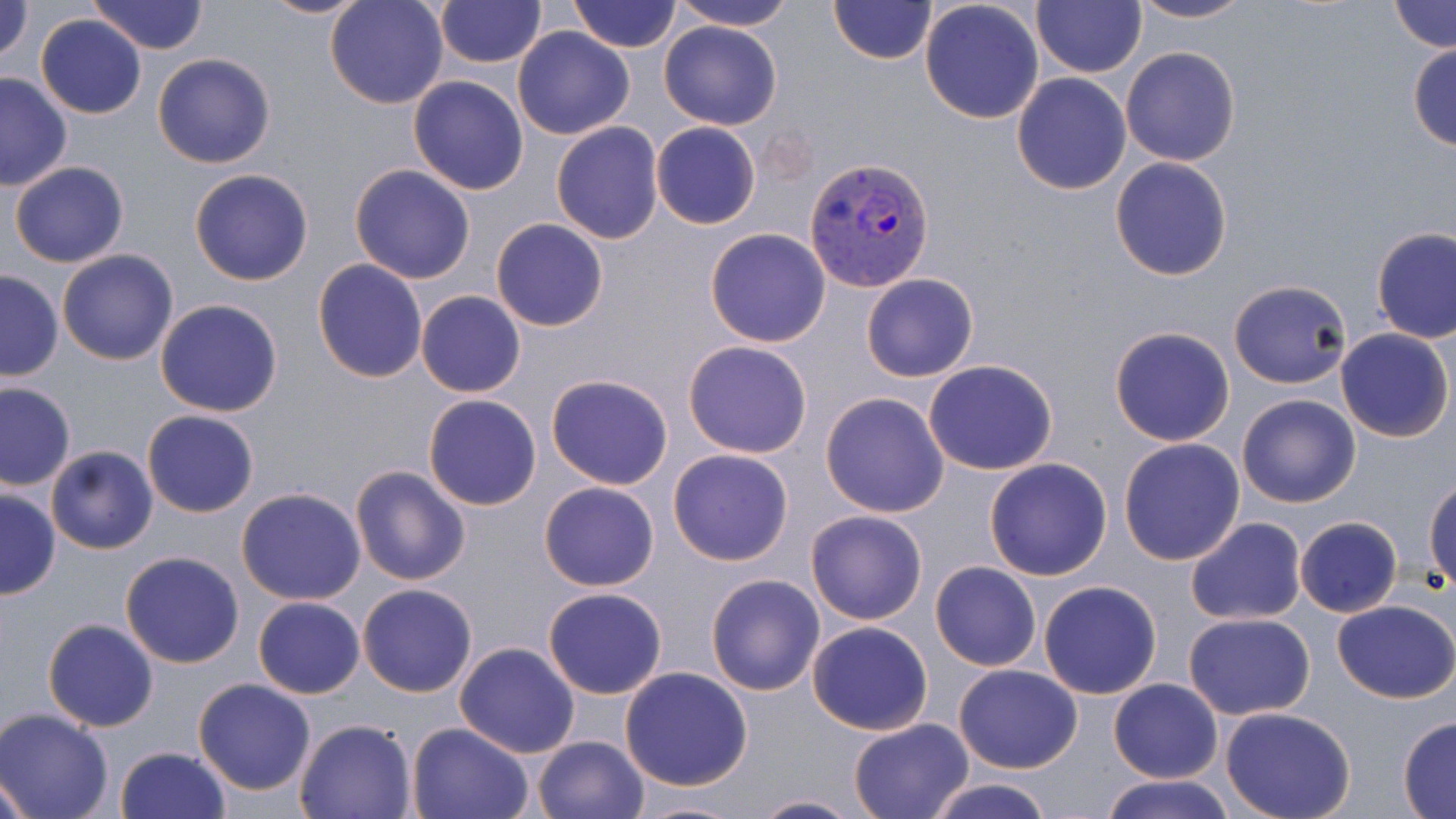 Approximate bounding boxes as (x1, y1, x2, y2) in pixels. Uninfected red blood cell locations: (0, 0, 34, 64), (88, 0, 209, 54), (257, 0, 370, 18), (324, 0, 451, 109), (433, 0, 544, 68), (569, 0, 683, 54), (670, 0, 798, 31), (828, 0, 938, 66), (839, 0, 1011, 90), (1032, 0, 1146, 78), (1127, 0, 1257, 25), (919, 1, 1045, 124), (1389, 1, 1454, 52), (36, 13, 147, 119), (658, 20, 782, 130), (512, 27, 635, 141), (1408, 42, 1456, 151), (1121, 46, 1240, 166), (151, 54, 275, 170), (0, 71, 74, 192), (1011, 72, 1132, 195), (408, 75, 529, 194), (550, 121, 665, 244), (651, 122, 761, 229), (1110, 157, 1233, 280), (9, 160, 129, 268), (349, 164, 475, 283), (189, 169, 314, 286), (491, 219, 609, 332), (1372, 227, 1456, 343), (704, 228, 832, 348), (57, 249, 179, 366), (312, 260, 427, 384), (0, 270, 64, 381), (861, 273, 979, 382), (1227, 280, 1354, 388), (416, 290, 525, 398), (154, 298, 283, 417), (1109, 326, 1235, 446), (1334, 328, 1453, 443), (683, 339, 813, 458), (923, 359, 1059, 475), (545, 373, 674, 490), (0, 380, 75, 491), (820, 392, 950, 517), (423, 393, 543, 510), (1236, 393, 1360, 509), (142, 408, 259, 519), (1119, 438, 1245, 565), (45, 443, 159, 555), (668, 448, 794, 567), (983, 458, 1113, 580), (349, 465, 470, 585), (1425, 477, 1456, 589), (539, 481, 659, 592), (0, 488, 61, 600), (236, 489, 366, 605), (805, 509, 929, 626), (1295, 516, 1402, 619), (1185, 518, 1308, 623), (120, 551, 245, 669), (930, 562, 1041, 671), (705, 572, 826, 695), (1037, 580, 1163, 700), (357, 583, 479, 698), (542, 586, 668, 699), (253, 596, 364, 699), (1332, 600, 1456, 703), (1183, 613, 1315, 719), (44, 618, 158, 731), (806, 621, 933, 736), (454, 641, 581, 757), (952, 664, 1083, 774), (619, 667, 754, 791), (192, 677, 318, 799), (1108, 679, 1223, 783), (1220, 708, 1355, 819), (0, 710, 116, 819), (294, 717, 418, 818), (847, 717, 975, 819), (1398, 717, 1456, 817), (404, 721, 534, 819), (532, 735, 652, 819), (115, 744, 231, 819), (1, 773, 32, 818), (1101, 773, 1237, 819), (920, 777, 1061, 819), (747, 794, 864, 819), (628, 798, 749, 819). Plasmodium vivax-infected red blood cell locations: (805, 156, 935, 291). Slide-level diagnosis: Plasmodium vivax. Light microscopy. Image is 1456×819 pixels. Thin blood smear. Single field of view. 1000x magnification. May-Grünwald-Giemsa stain.